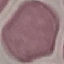
malaria status = uninfected
capture = smartphone camera at the microscope eyepiece
stain = Giemsa
image type = cell patch, automatically extracted from a larger field of view and resized to 64 × 64 pixels
preparation = thin blood smear